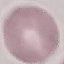
Malaria status: uninfected. Thin blood smear. Photographed with a smartphone camera at the microscope eyepiece. Giemsa stain. Automatically extracted cell patch, resized to 64 × 64 pixels.